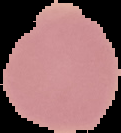
image type = segmented cell region on a black background
preparation = thin blood smear
result = no malaria parasites detected
image size = 121×133 pixels